Assess the morphology of the erythrocytes.
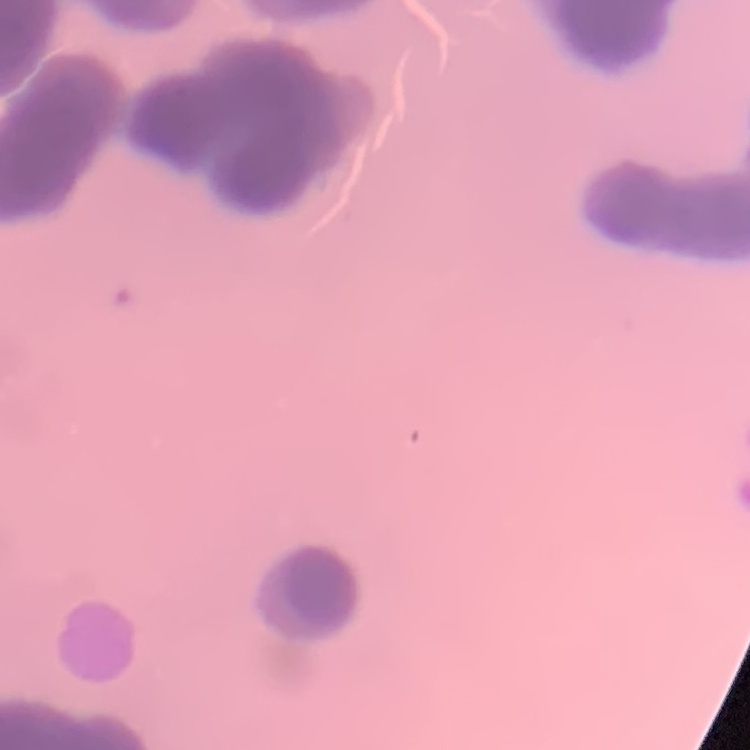
Rouleaux formation.

Summary:
  - Stain: Field's or Giemsa
  - Image type: square crop of a larger photomicrograph
  - Preparation: thin peripheral smear